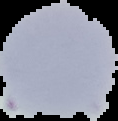
The area outside the segmented cell region is set to black. From a thin blood smear. Malaria status: uninfected. Image is 118×121 pixels.